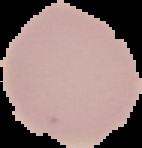
Summary:
  - Image type: segmented cell region with the area outside set to black
  - Image size: 142×148 pixels
  - Preparation: thin blood smear
  - Malaria status: uninfected